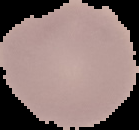

{
  "malaria_status": "uninfected",
  "image_size": "139×130 pixels",
  "image_type": "cell region segmented out of the field of view; surrounding area masked to black",
  "preparation": "thin blood smear"
}